Assess this cell for malaria.
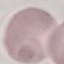

It is uninfected.

Summary:
  - Stain: Giemsa
  - Preparation: thin smear
  - Image type: cell patch, automatically extracted from a larger field of view and resized to 64 × 64 pixels
  - Capture: smartphone through the microscope eyepiece